Point out each malaria parasite.
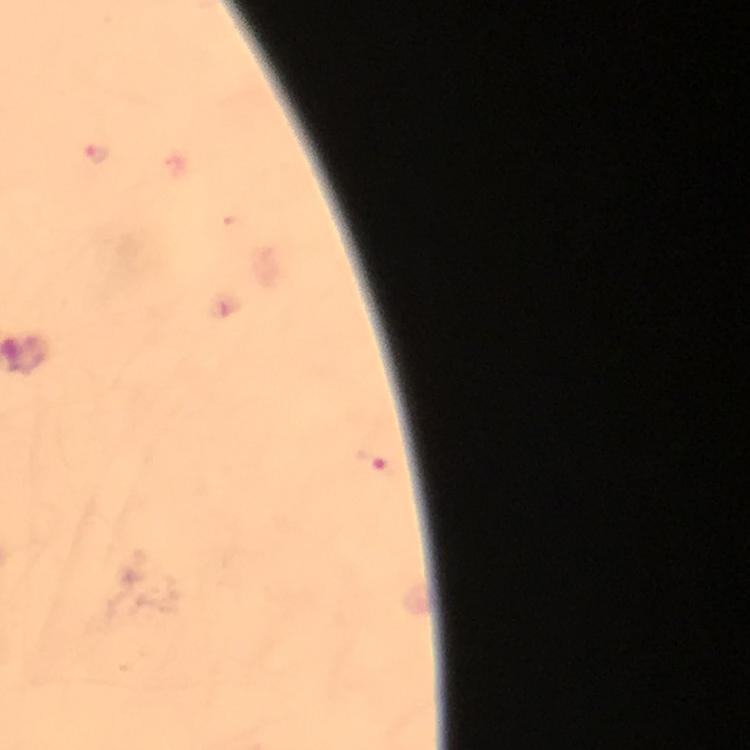

Approximate centers as [x, y] in pixels.
Malaria parasites: [97, 153], [371, 461].

cropped from = a single field of view
context = from a malaria diagnostic workup
capture = smartphone photograph through a microscope
immersion oil = used
preparation = thick blood smear
magnification = 100x
image size = 750×750 pixels
stain = Giemsa